Identify the cell.
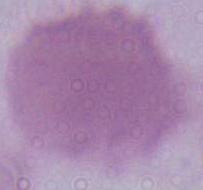
An erythrocyte.

modality = photomicrograph
magnification = 1000x